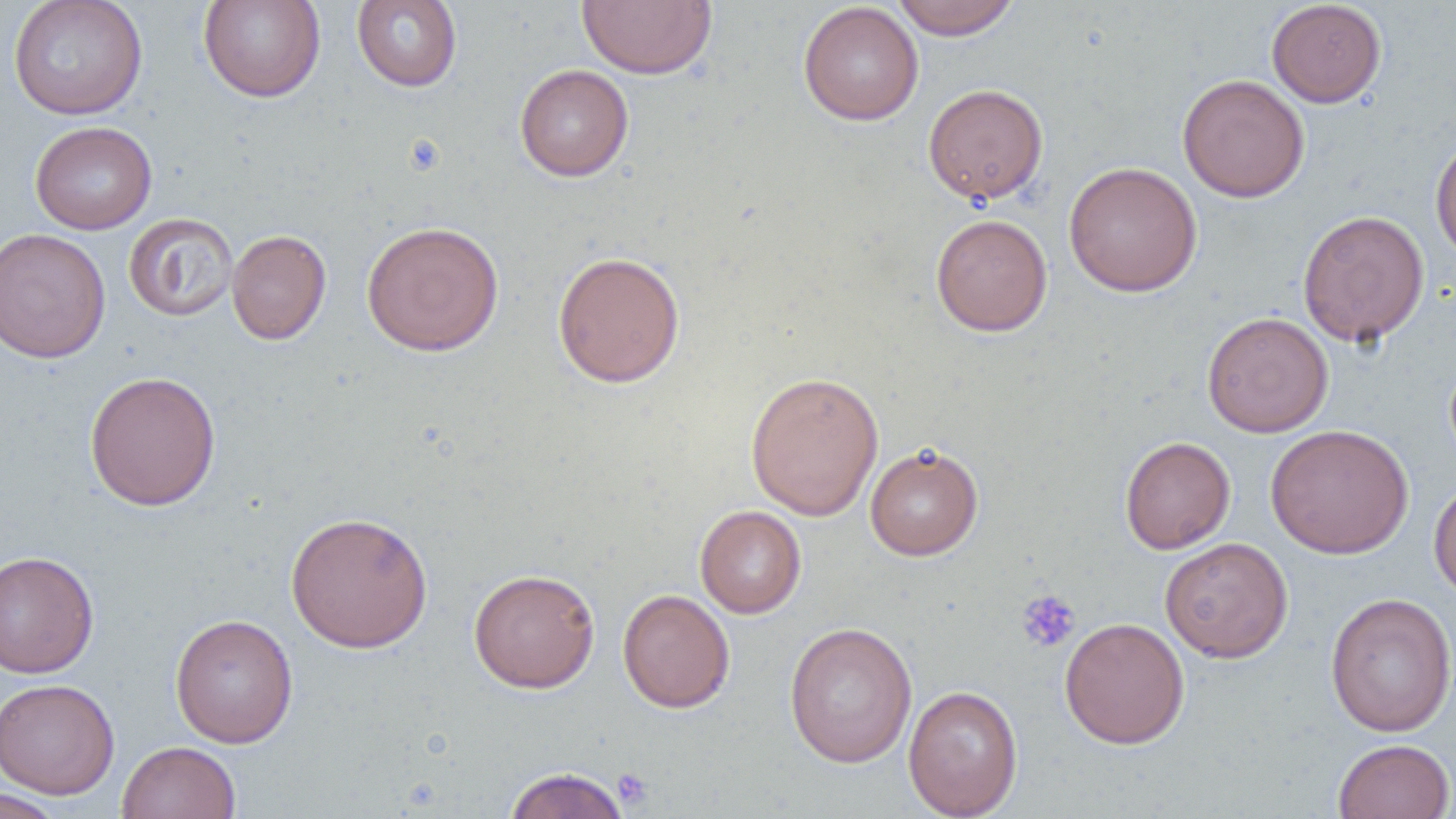
Approximate bounding boxes as (x1,y1)-(x2,y2) corner pairs in pixels. Uninfected red blood cell locations: (8,0)-(148,120), (197,0)-(326,102), (351,0)-(462,91), (577,0)-(717,79), (890,0)-(1021,39), (1266,1)-(1386,108), (797,2)-(924,126), (515,64)-(633,181), (1177,74)-(1310,203), (923,83)-(1048,205), (30,120)-(157,234), (1430,132)-(1456,263), (1063,161)-(1202,297), (1297,209)-(1430,346), (124,213)-(239,322), (931,214)-(1052,336), (361,221)-(504,356), (0,228)-(111,363), (226,229)-(331,345), (552,250)-(686,388), (1202,311)-(1333,437), (84,370)-(221,511), (744,371)-(884,520), (1265,424)-(1414,559), (1120,436)-(1235,553), (864,442)-(983,560), (1429,477)-(1456,602), (694,505)-(806,618), (285,510)-(433,653), (1159,537)-(1294,663), (0,550)-(99,678), (468,567)-(600,692), (617,588)-(735,712), (1325,592)-(1456,737), (169,613)-(298,747), (1059,617)-(1190,749), (784,621)-(918,767), (0,678)-(120,799), (903,684)-(1023,819), (1332,738)-(1455,819), (116,741)-(241,819), (502,766)-(631,819), (0,788)-(67,819). Platelet locations: (1016,589)-(1080,653), (612,767)-(654,809). Slide-level diagnosis: negative for blood parasites. Light microscopy. One field of a larger specimen. Thin blood smear. Captured at 1000x magnification. Image is 1456×819 pixels.